Rate the background quality.
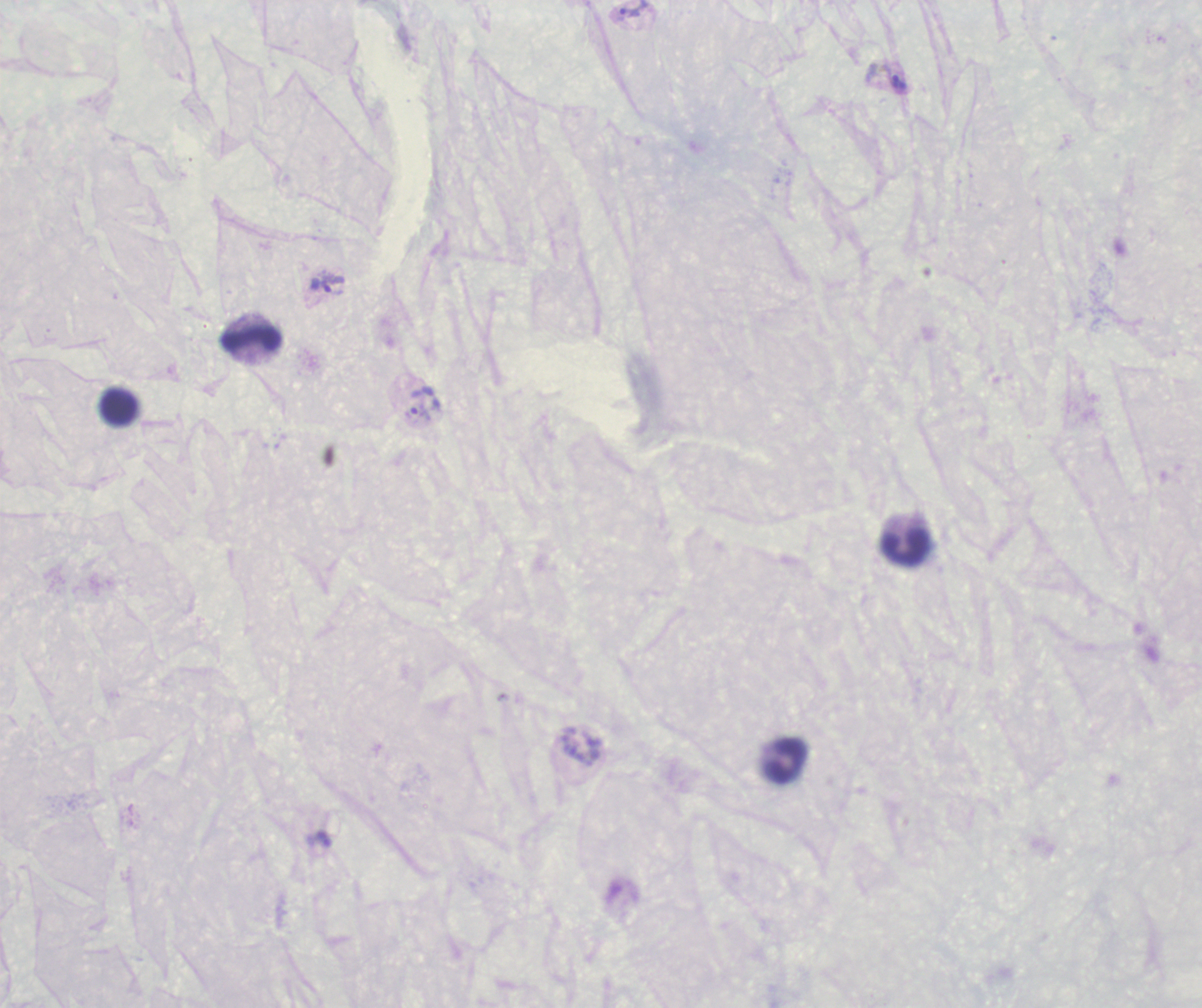
It is poor.

Approximate centers as {x, y} in pixels. Leukocyte locations: {251, 338}, {118, 407}, {904, 547}, {785, 759}. Trophozoite locations: {634, 9}, {898, 82}, {327, 284}, {425, 399}. Previously used in a real diagnosis. Single field of view. Thick smear of blood. Romanowsky stain. Coloration quality: bad. Image is 1202×1008 pixels. Result: Plasmodium parasites identified. Captured at 100x magnification.